Name the blood parasite species.
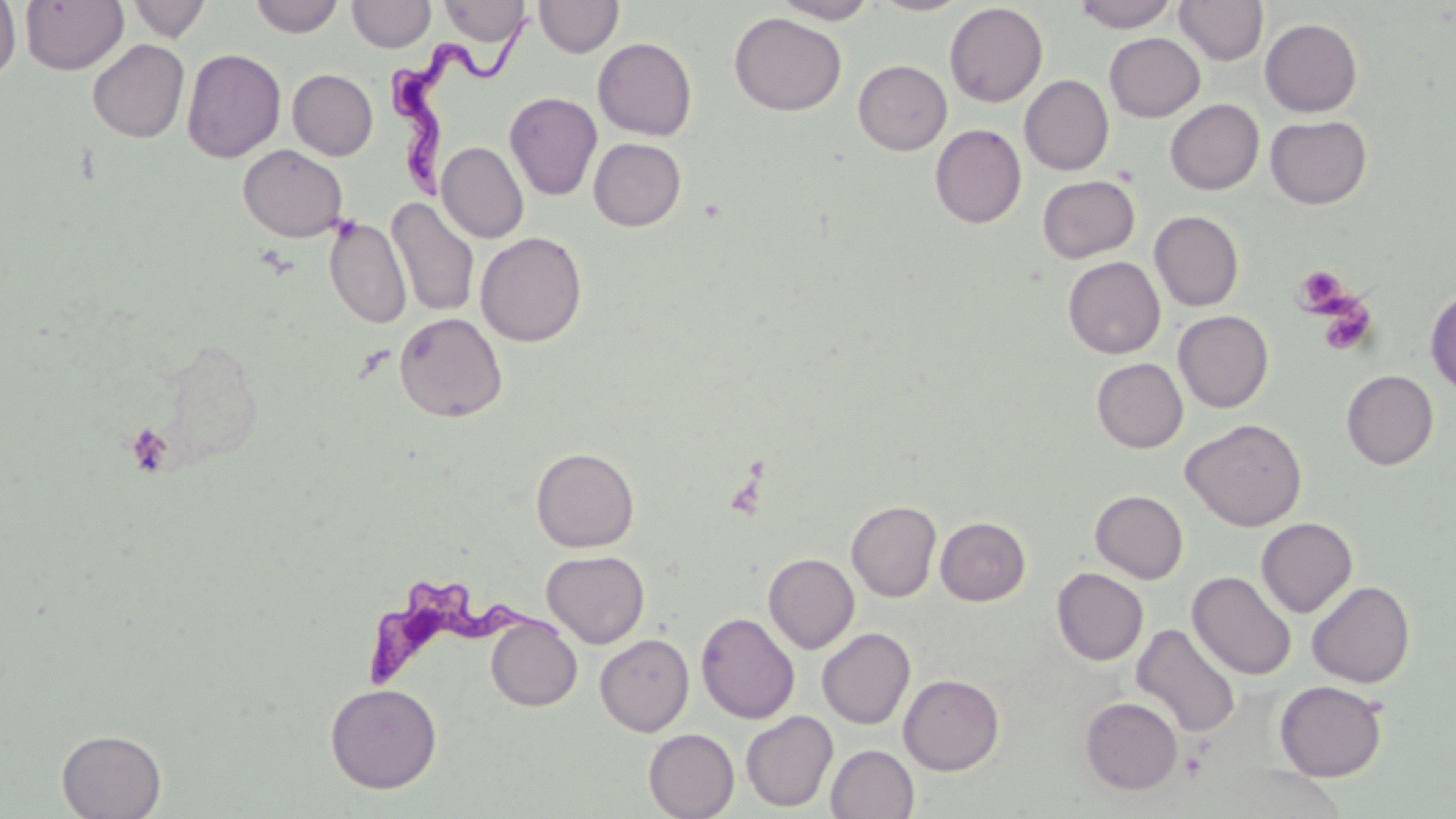

Trypanosoma brucei.

Approximate bounding boxes as [x1, y1, x2, y2] in pixels. Platelet locations: [1294, 265, 1348, 313], [1318, 300, 1377, 356], [125, 422, 174, 477]. Trypanosoma brucei locations: [383, 3, 546, 198], [363, 569, 580, 694]. Uninfected red blood cell locations: [0, 0, 21, 83], [20, 0, 128, 74], [128, 0, 211, 42], [249, 0, 344, 38], [347, 0, 435, 53], [534, 0, 623, 58], [772, 0, 879, 24], [871, 0, 971, 16], [1074, 0, 1179, 32], [1175, 0, 1268, 66], [438, 1, 531, 47], [944, 2, 1048, 107], [730, 13, 846, 115], [1260, 18, 1363, 117], [1104, 33, 1205, 122], [593, 37, 697, 141], [87, 39, 189, 143], [182, 48, 286, 163], [853, 60, 952, 155], [287, 69, 378, 160], [1020, 75, 1114, 175], [504, 91, 602, 201], [1165, 99, 1264, 195], [1265, 115, 1372, 209], [930, 124, 1026, 228], [589, 138, 686, 231], [437, 142, 528, 243], [238, 145, 349, 242], [1037, 174, 1140, 264], [386, 196, 480, 318], [1150, 210, 1244, 311], [324, 217, 412, 330], [475, 231, 587, 346], [1063, 256, 1166, 358], [1425, 286, 1456, 396], [1173, 310, 1273, 413], [394, 312, 508, 423], [1091, 358, 1187, 453], [1341, 370, 1439, 470], [1181, 418, 1307, 531], [531, 446, 639, 552], [1090, 490, 1188, 584], [846, 499, 941, 602], [935, 516, 1031, 605], [1256, 517, 1358, 618], [542, 550, 650, 648], [763, 553, 859, 653], [1052, 568, 1148, 665], [1187, 571, 1297, 680], [1307, 580, 1415, 688], [696, 612, 800, 724], [485, 616, 582, 711], [1132, 623, 1242, 738], [817, 628, 915, 729], [595, 634, 694, 736], [898, 674, 1005, 775], [1274, 680, 1388, 781], [325, 682, 443, 794], [1080, 697, 1183, 795], [741, 711, 838, 812], [644, 728, 739, 819], [56, 729, 167, 818], [826, 745, 919, 818]. Captured at 1000x magnification. One field of a larger specimen. Thin blood smear. Optical microscopy. May-Grünwald-Giemsa stain. Image is 1456×819 pixels.